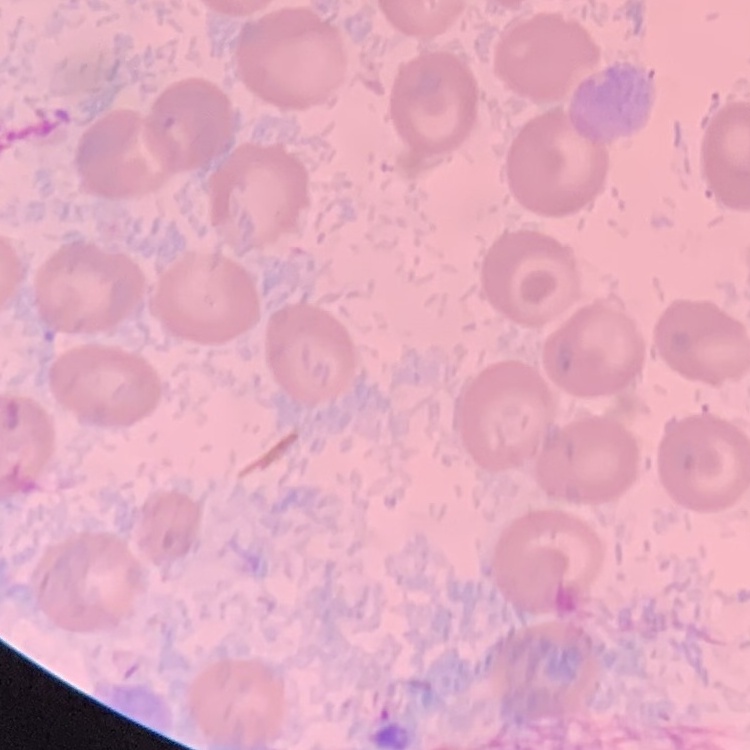

Summary:
  - Red blood cell morphology: no rouleaux formation
  - Preparation: thin peripheral smear
  - Image type: one tile cut from a larger photomicrograph
  - Stain: Field's or Giemsa